Report the malaria status of this cell.
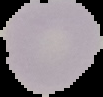

Uninfected.

{
  "image_size": "103×97 pixels",
  "image_type": "segmented cell region on a black background",
  "preparation": "thin blood smear"
}